Locate every malaria parasite by life-cycle stage, and every leukocyte.
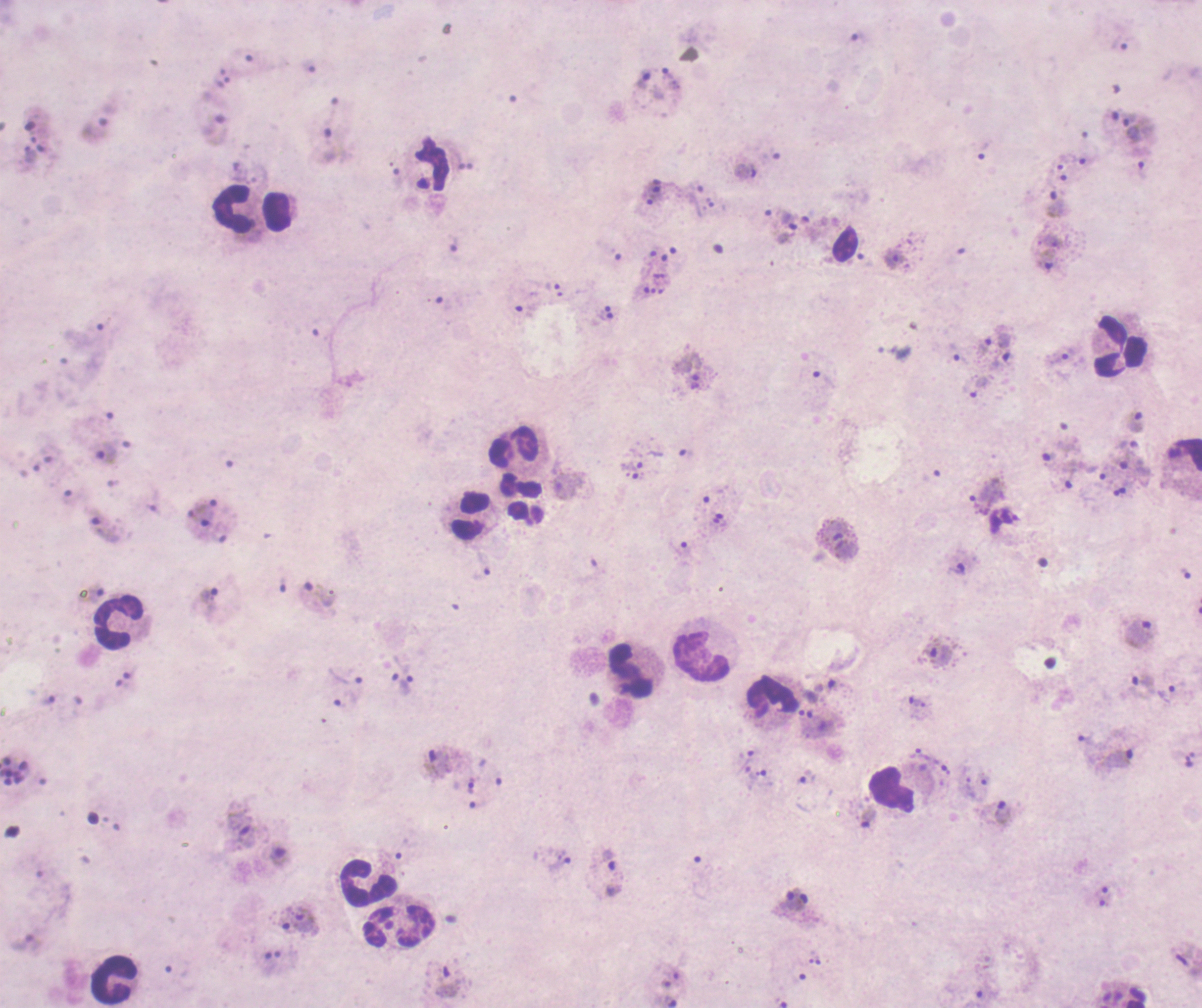
Approximate centers as [x, y] in pixels.
Trophozoites: [856, 37], [1120, 45], [644, 81], [99, 122], [1132, 128], [214, 130], [984, 151], [1083, 155], [1142, 170], [744, 171], [1056, 204], [787, 220], [453, 244], [894, 259], [1046, 259], [997, 339], [1061, 355], [958, 358], [980, 384], [1136, 421], [103, 451], [987, 494], [105, 528], [955, 569], [318, 593], [206, 603], [1139, 632], [939, 657], [345, 676], [1142, 680], [409, 683], [1166, 693], [919, 752], [1118, 758], [440, 761], [807, 777], [1002, 812], [240, 827], [278, 854], [610, 859], [557, 864], [613, 890], [297, 918], [448, 983].
No schizont or gametocyte forms observed.
Leukocytes: [233, 208], [276, 210], [1118, 348], [513, 448], [470, 516], [118, 625], [702, 656], [631, 670], [770, 698], [892, 790], [367, 880], [398, 925], [114, 981].

Summary:
  - Magnification: 100x
  - Coloration quality: bad
  - Preparation: thick blood smear
  - Image size: 1202×1008 pixels
  - Stain: Romanowsky
  - Field of view: single
  - Context: previously used in a real diagnosis
  - Background quality: poor